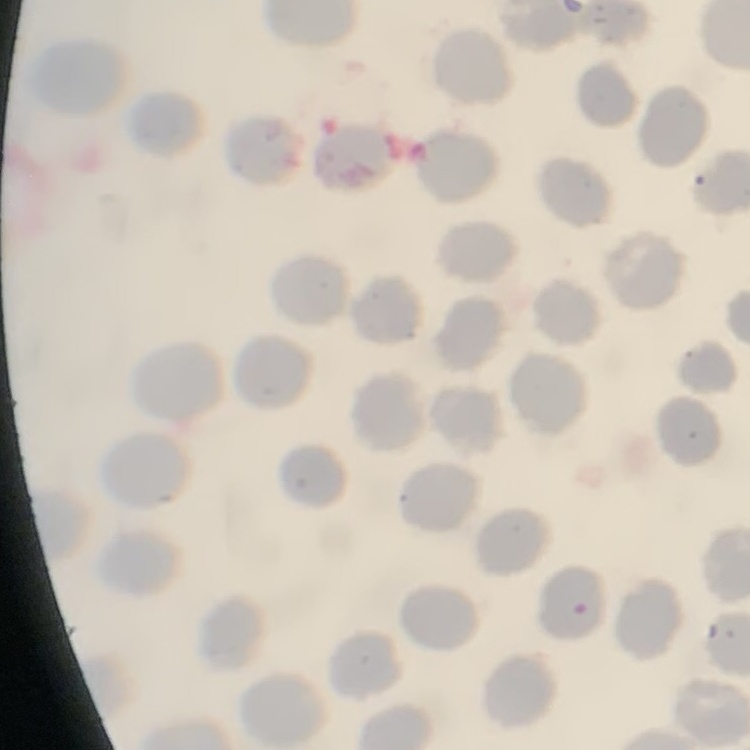
erythrocyte morphology = no rouleaux formation
stain = Field's or Giemsa
image type = square crop of a larger photomicrograph
preparation = thin blood smear